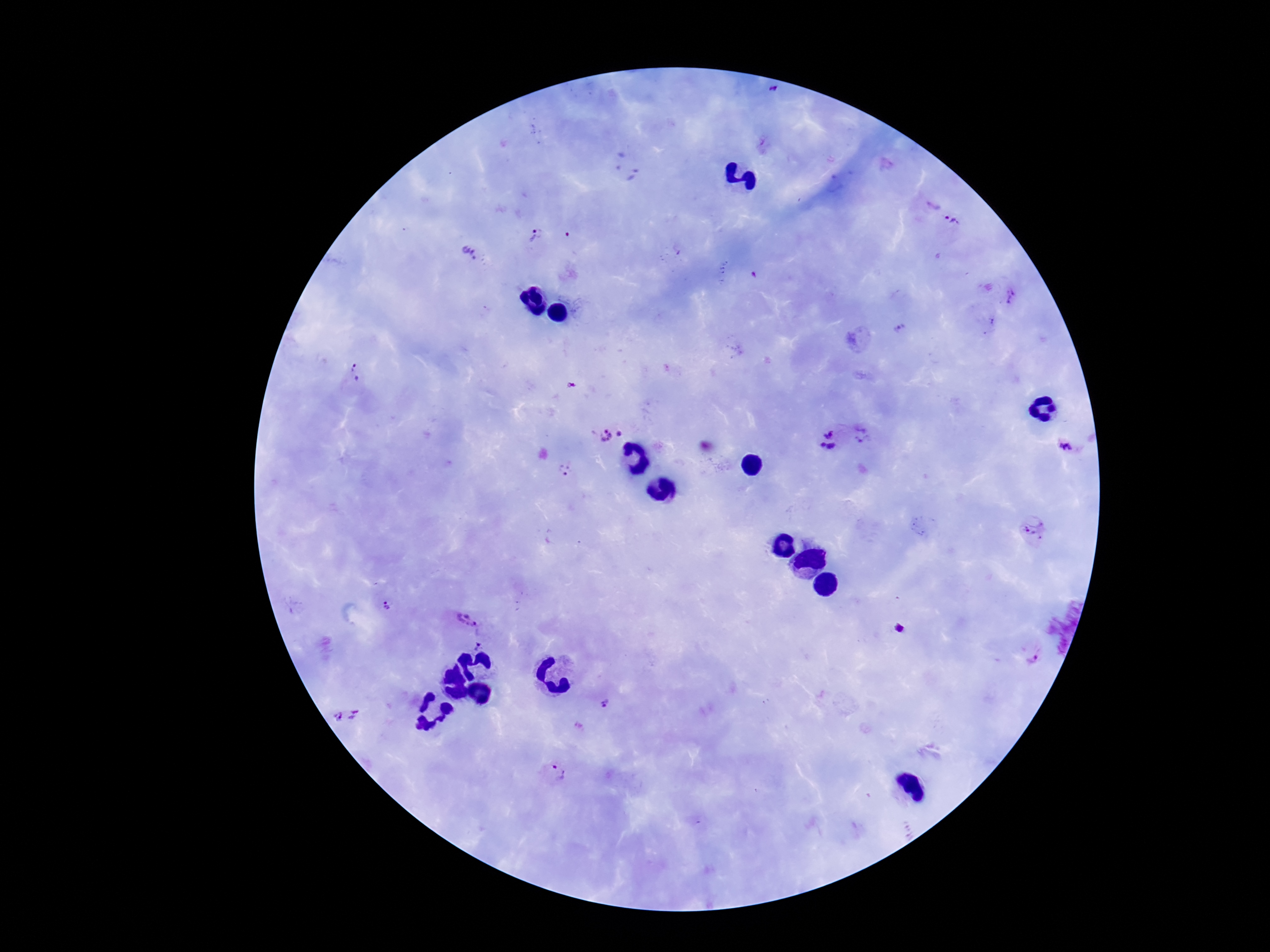

Approximate centers as (x, y) in pixels. Plasmodium parasite locations: (772, 89), (953, 221), (536, 236), (570, 237), (473, 253), (754, 275), (1011, 298), (989, 321), (902, 330), (858, 339), (358, 374), (609, 433), (870, 434), (832, 439), (1065, 446), (566, 468), (1034, 533), (388, 608), (466, 616), (899, 628), (482, 645), (1031, 650), (605, 706), (344, 719), (555, 772). Giemsa-stained preparation. Smartphone photograph taken through the microscope eyepiece. 100x magnification. Image is 1270×952 pixels. Patient malaria status: positive. One field from this slide. Thick blood smear.